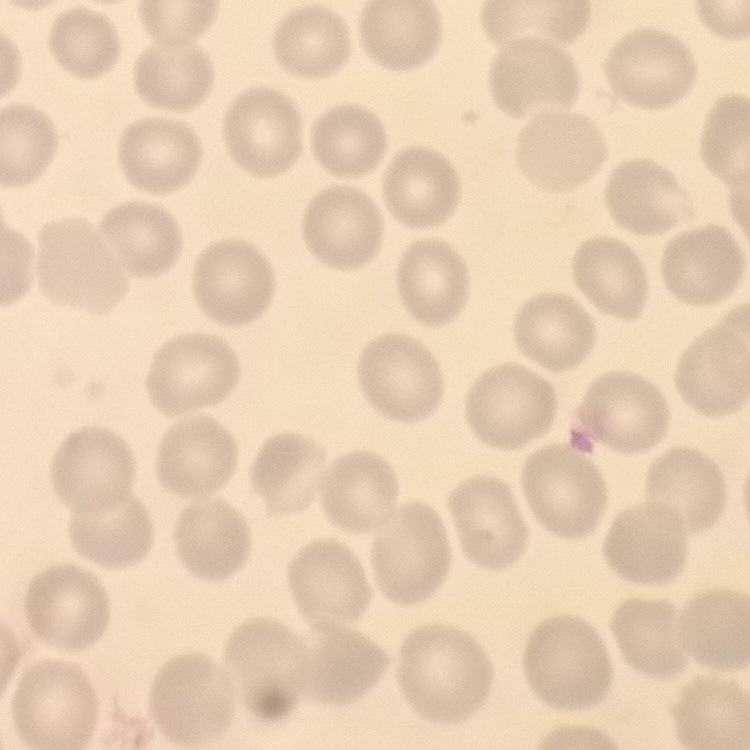

red_blood_cell_morphology: no rouleaux formation
preparation: thin blood smear
image_type: square crop of a larger photomicrograph
stain: Field's or Giemsa